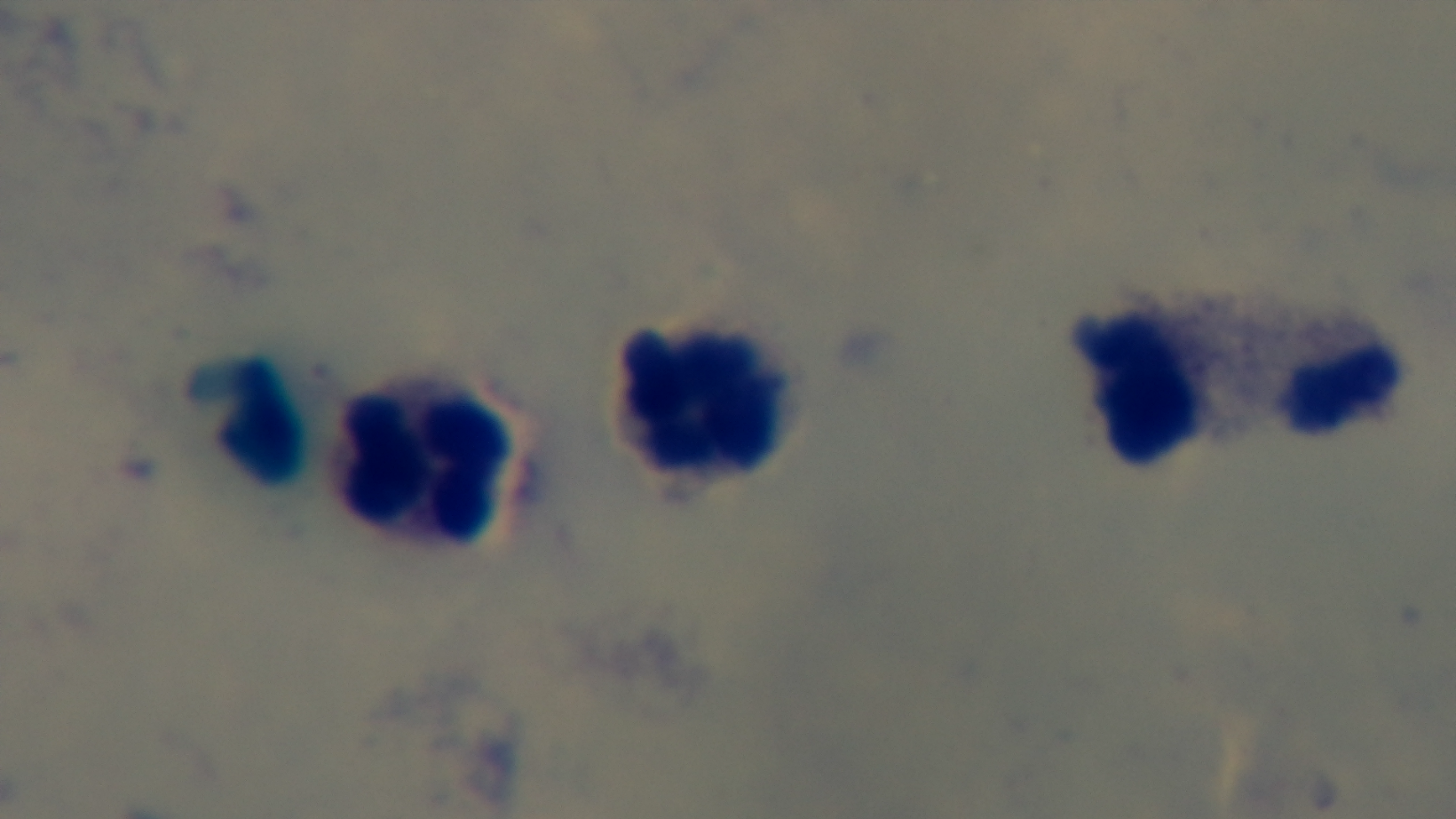

objective: 100x oil immersion
preparation: thick smear
stain: Giemsa
modality: light microscopy
capture: mounted 4K digital camera
field_of_view: one from the slide
malaria_status: negative